Give the position of every Plasmodium parasite.
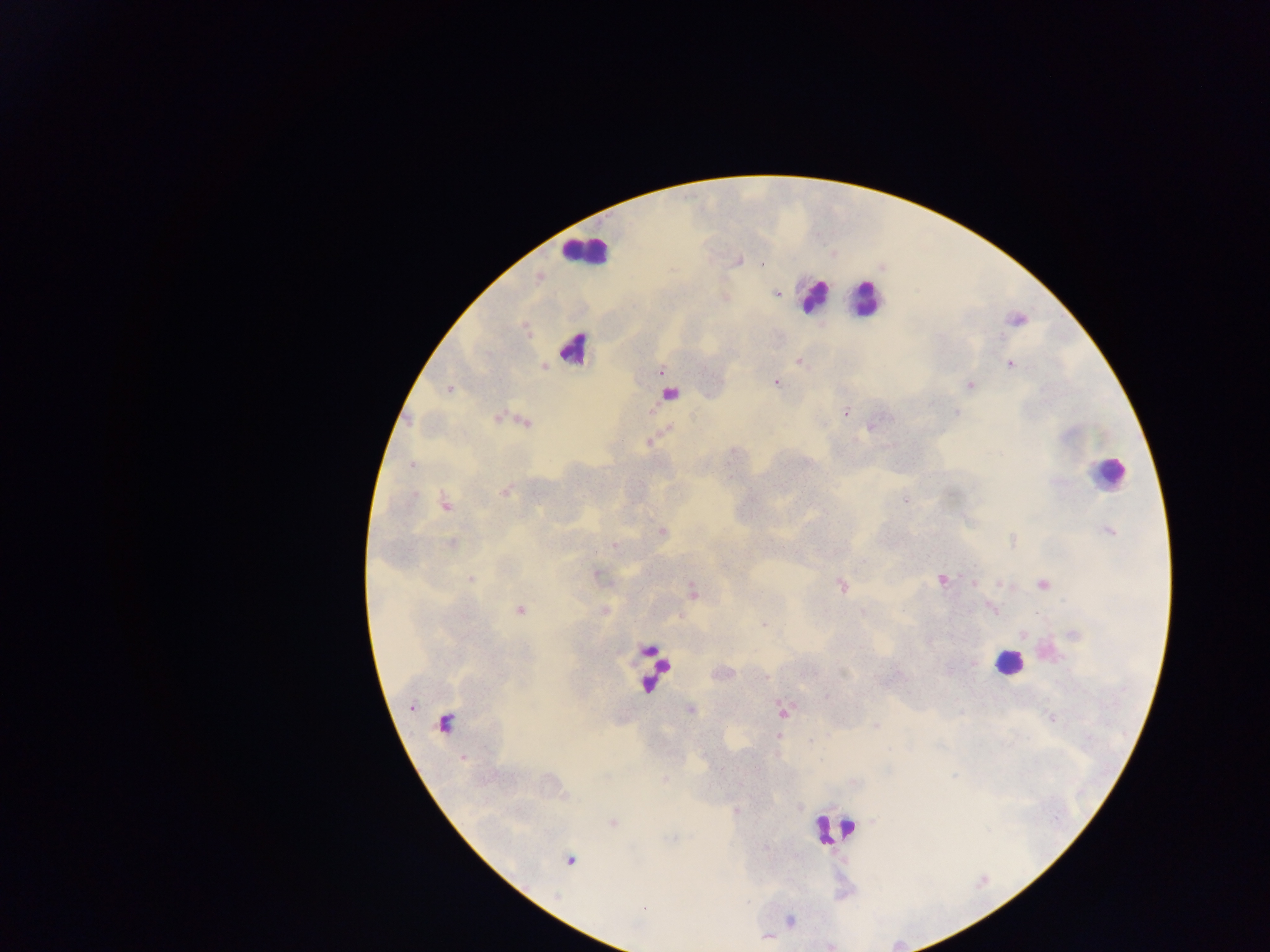

Approximate centers as x y in pixels.
Plasmodium parasites: 739 260; 762 264; 776 293; 725 297; 1017 319; 798 360; 1010 362; 545 367; 662 371; 776 383; 969 384; 449 389; 845 413; 499 417; 524 421; 872 425; 647 442; 411 465; 505 491; 444 503; 1108 530; 661 532; 1012 541; 452 544; 613 545; 597 574; 471 579; 941 580; 973 582; 1042 583; 841 584; 692 591; 519 608; 991 608; 604 610; 764 623; 1075 635; 690 709; 782 710; 1051 717; 443 723; 876 724; 463 758; 613 823; 569 859; 789 921; 766 936.

Leukocyte locations: 585 251; 813 296; 865 298; 573 348; 669 393; 1109 473; 1008 661; 654 670; 834 830. Thick blood film. Single field of view. Photographed through a microscope with a mobile-phone camera. Sample from Ghana. Image is 1270×952 pixels.